State which parasite is depicted.
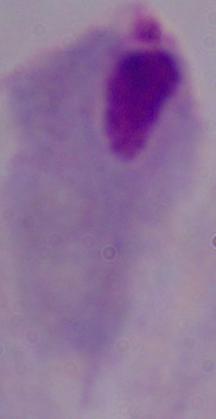
This is a trichomonad.

Photomicrograph. 1000x magnification.